Report the malaria status of this cell.
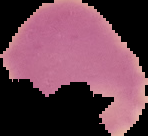

It is uninfected.

preparation = thin blood smear
image type = segmented cell region with the area outside set to black
image size = 148×136 pixels